Point out cells.
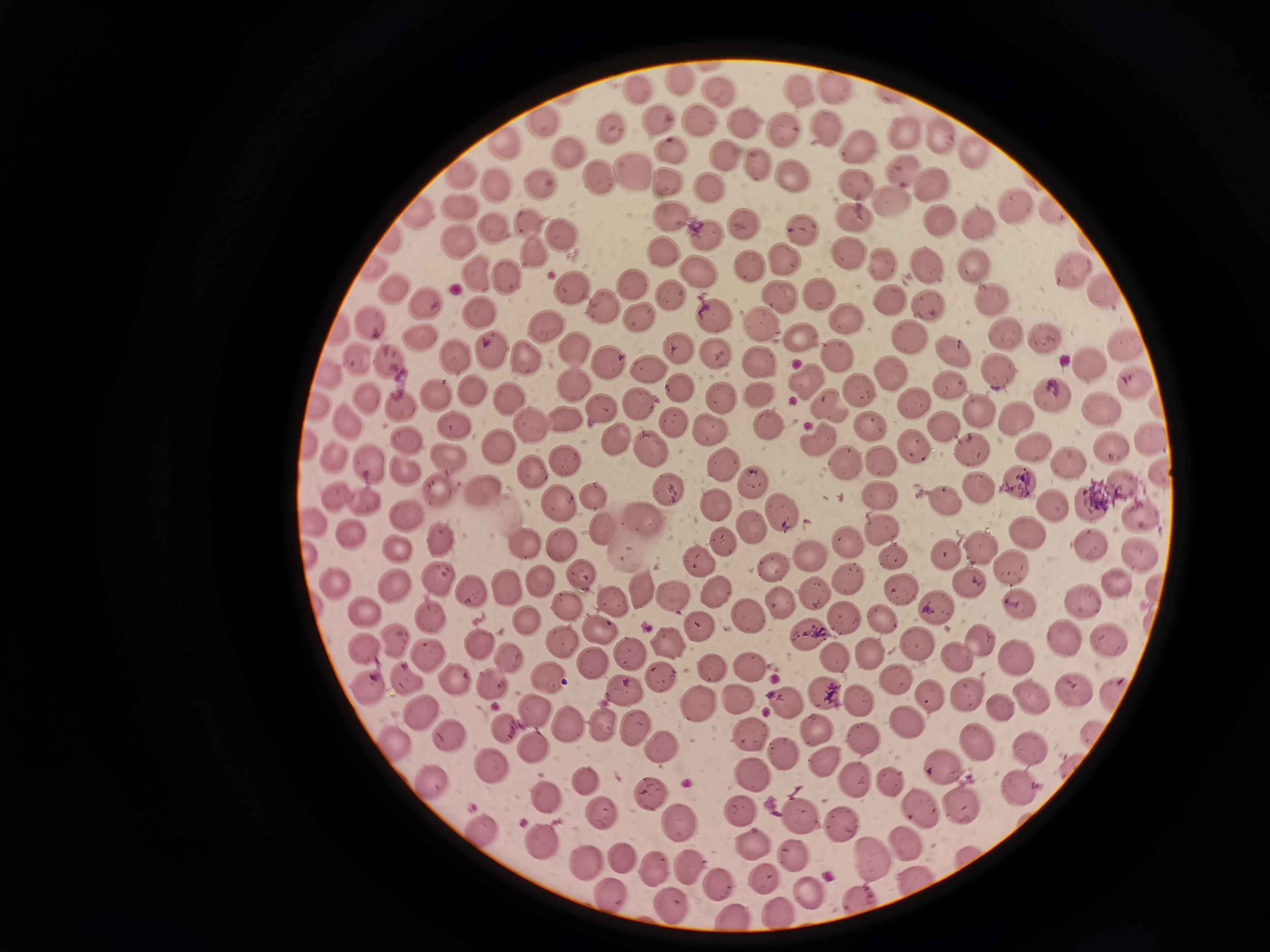

Approximate centers as [x, y] in pixels.
Cells: [681, 82], [834, 88], [641, 90], [798, 92], [720, 93], [702, 118], [662, 119], [539, 120], [743, 124], [825, 129], [782, 130], [614, 131], [940, 132], [902, 135], [503, 139], [855, 150], [967, 150], [572, 154], [723, 157], [756, 168], [901, 169], [463, 171], [633, 171], [789, 177], [599, 178], [667, 181], [928, 183], [543, 185], [496, 186], [854, 187], [709, 190], [892, 201], [461, 207], [1013, 207], [417, 213], [672, 217], [850, 219], [980, 220], [530, 222], [943, 222], [745, 225], [494, 227], [800, 229], [557, 234], [708, 235], [456, 242], [665, 252], [535, 255], [780, 256], [851, 256], [879, 264], [931, 264], [749, 266], [973, 266], [697, 271], [1072, 271], [479, 273], [511, 276], [634, 283], [395, 289], [816, 291], [1104, 292], [572, 293], [671, 295], [775, 296], [889, 299], [602, 302], [427, 304], [926, 304], [992, 304], [482, 311], [844, 318], [641, 319], [713, 319], [370, 324], [760, 326], [543, 327], [1045, 334], [906, 335], [801, 337], [419, 341], [1009, 341], [679, 346], [1122, 346], [575, 347], [492, 349], [718, 352], [953, 352], [451, 356], [519, 356], [838, 357], [359, 358], [391, 360], [756, 360], [1090, 361], [606, 364], [998, 369], [654, 371], [889, 372], [805, 382], [573, 385], [1134, 386], [681, 387], [474, 390], [949, 390], [861, 392], [1048, 394], [508, 395], [366, 397], [718, 397], [758, 397], [640, 404], [915, 404], [1102, 406], [832, 407], [402, 408], [601, 412], [980, 413], [1015, 416], [568, 419], [345, 421], [452, 422], [767, 423], [939, 425], [872, 426], [529, 427], [710, 428], [1150, 436], [408, 440], [816, 441], [619, 442], [501, 445], [914, 446], [1112, 446], [332, 451], [651, 451], [967, 452], [1033, 452], [451, 458], [564, 459], [724, 459], [849, 463], [882, 463], [1068, 464], [372, 468], [533, 472], [1158, 472], [1017, 481], [753, 482], [665, 485], [440, 487], [973, 489], [488, 491], [333, 496], [594, 496], [882, 496], [1090, 501], [1052, 502], [949, 503], [364, 504], [714, 505], [564, 506], [779, 513], [405, 514], [643, 514], [1141, 518], [604, 526], [745, 526], [884, 531], [348, 533], [1030, 534], [442, 541], [724, 542], [525, 543], [845, 543], [561, 545], [978, 545], [1090, 545], [394, 547], [893, 553], [944, 555], [809, 558], [1139, 559], [698, 561], [1009, 564], [773, 568], [583, 577], [438, 578], [845, 579], [971, 582], [540, 583], [331, 584], [1120, 586], [715, 587], [900, 587], [395, 588], [507, 588], [642, 590], [471, 591], [813, 595], [617, 597], [673, 597], [779, 601], [1081, 601], [935, 605], [1024, 605], [570, 608], [363, 610], [748, 615], [843, 618], [882, 618], [432, 619], [528, 619], [602, 629], [703, 630], [812, 637], [1069, 638], [398, 640], [1107, 640], [477, 642], [669, 642], [915, 642], [980, 643], [564, 646], [367, 649], [630, 653], [870, 655], [1016, 655], [509, 656], [835, 657], [957, 657], [427, 659], [593, 661], [748, 666], [707, 667], [457, 676], [659, 677], [544, 679], [409, 681], [895, 681], [494, 684], [371, 687], [624, 689], [1069, 691], [829, 697], [1035, 697], [782, 699], [930, 699], [968, 699], [858, 700], [740, 701], [702, 702], [999, 703], [532, 710], [414, 713], [910, 723], [601, 724], [566, 725], [635, 728], [507, 729], [816, 731], [449, 734], [750, 735], [862, 737], [394, 740], [533, 745], [975, 746], [661, 747], [1028, 749], [781, 757], [825, 761], [492, 762], [944, 769], [749, 776], [852, 780], [429, 781], [588, 783], [893, 785], [1014, 787], [649, 795], [549, 798], [962, 806], [922, 811], [741, 813], [602, 815], [802, 815], [678, 822], [843, 824], [482, 827], [545, 843], [905, 843], [794, 857], [873, 857], [624, 858], [589, 864], [656, 867], [690, 867], [766, 879], [717, 883], [806, 890], [612, 892], [670, 904], [732, 914].

field of view = single
image size = 1270×952 pixels
preparation = thin blood smear
capture = smartphone through the microscope eyepiece
stain = Giemsa